Comment on the morphology of the red blood cells.
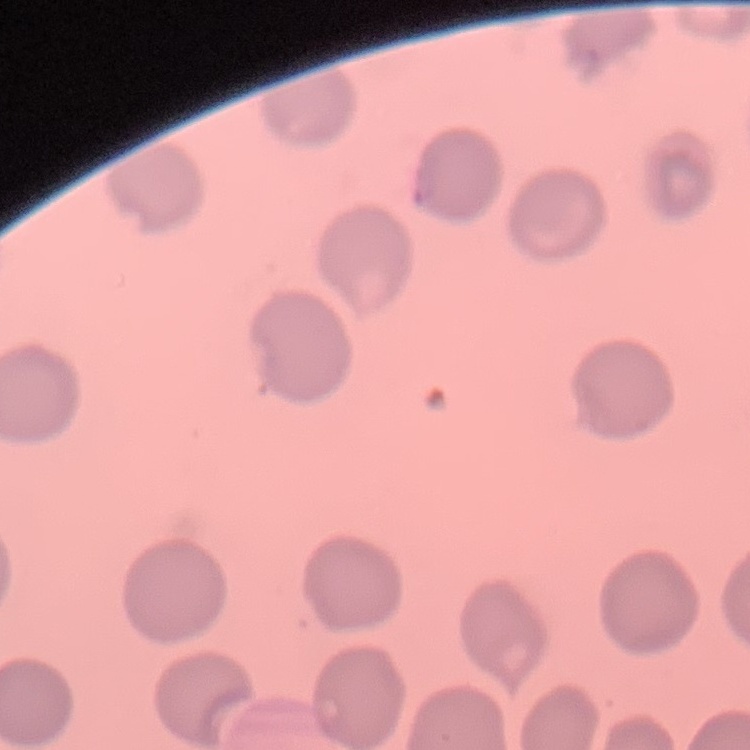

No rouleaux formation.

image type = one tile cut from a larger photomicrograph
preparation = thin blood smear
stain = Field's or Giemsa